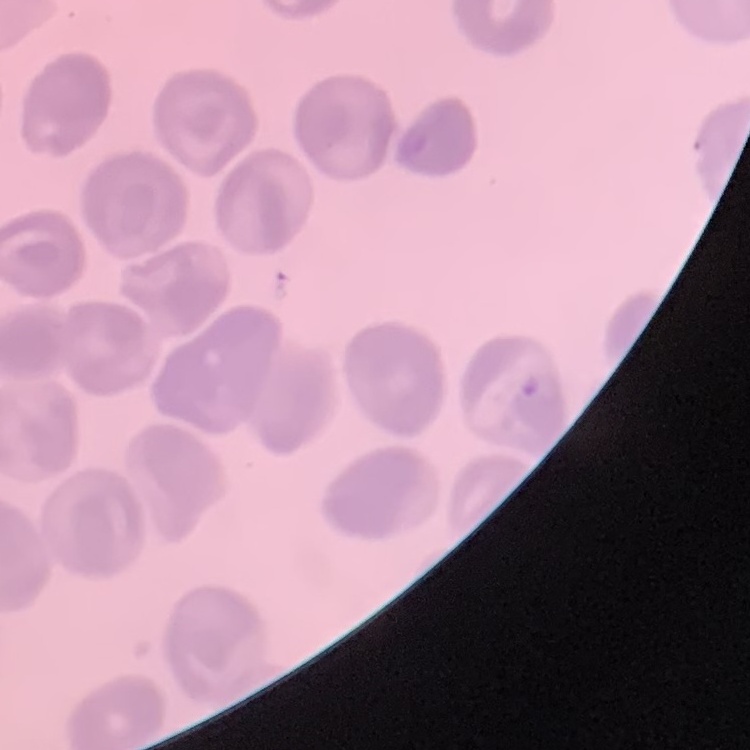

{
  "red_blood_cell_morphology": "no rouleaux formation",
  "image_type": "one tile cut from a larger photomicrograph",
  "stain": "Field's or Giemsa",
  "preparation": "thin blood film"
}